Name the blood parasite species.
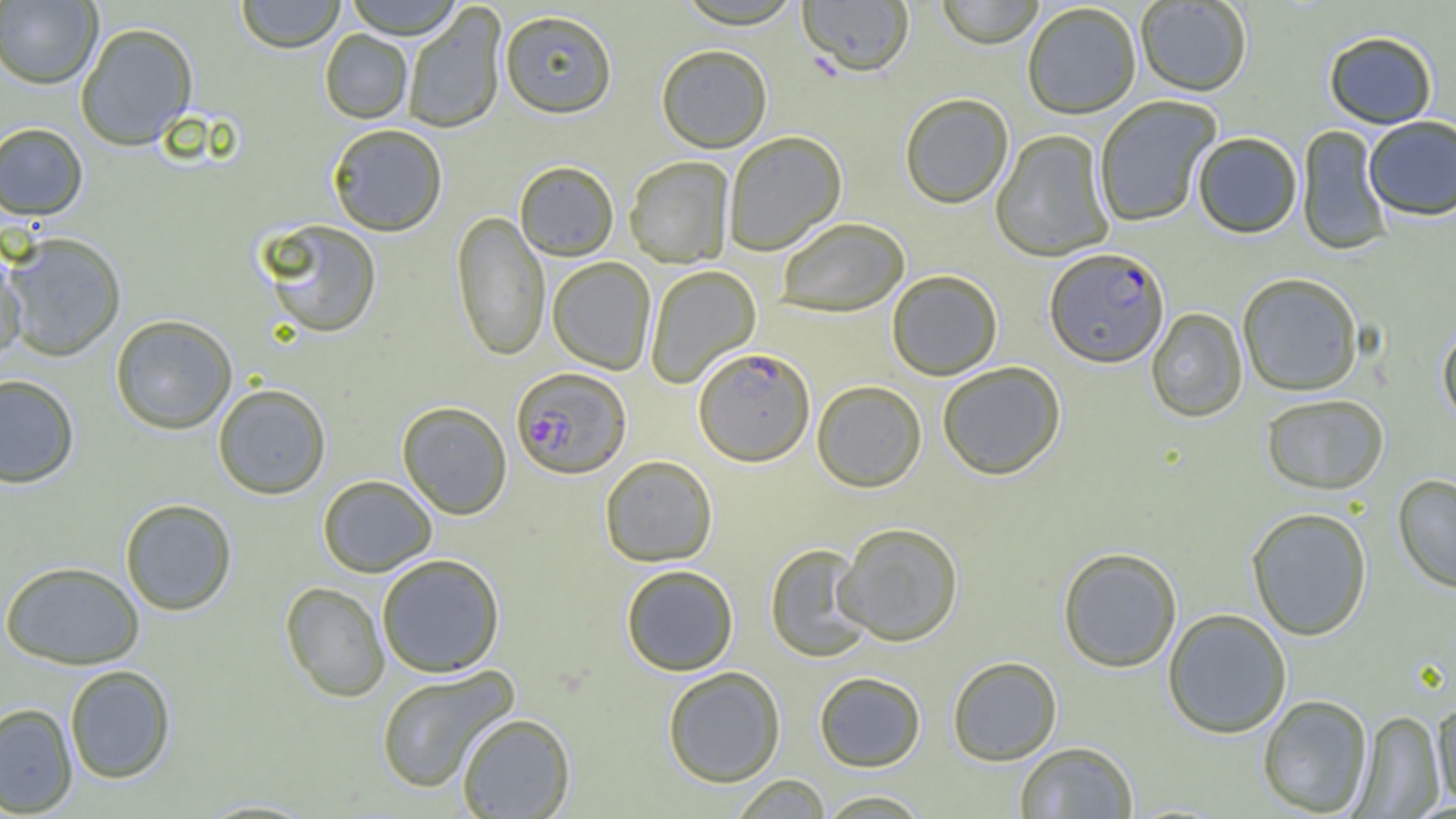

Plasmodium falciparum.

Approximate bounding boxes as (x1, y1, x2, y2) in pixels. Plasmodium falciparum-infected red blood cell locations: (1044, 249, 1169, 370), (693, 347, 815, 467), (510, 366, 631, 480). Uninfected red blood cell locations: (236, 0, 345, 52), (343, 0, 464, 38), (676, 0, 804, 30), (797, 0, 915, 80), (935, 0, 1045, 50), (0, 1, 102, 88), (1136, 1, 1252, 98), (402, 4, 507, 134), (1022, 4, 1141, 121), (499, 10, 618, 119), (75, 22, 198, 150), (320, 29, 413, 123), (1323, 31, 1438, 130), (656, 45, 772, 154), (900, 94, 1014, 210), (1094, 97, 1221, 227), (1364, 118, 1456, 222), (0, 122, 88, 221), (327, 123, 448, 236), (1296, 126, 1393, 257), (992, 131, 1115, 263), (723, 132, 847, 255), (1193, 133, 1302, 239), (624, 157, 734, 268), (514, 161, 619, 261), (452, 210, 550, 362), (777, 218, 910, 317), (258, 219, 383, 338), (2, 232, 127, 362), (0, 248, 27, 365), (547, 257, 656, 375), (645, 265, 761, 389), (887, 271, 1003, 381), (1237, 274, 1363, 397), (1146, 308, 1247, 423), (110, 314, 238, 434), (1437, 322, 1456, 431), (937, 362, 1066, 481), (0, 374, 80, 488), (812, 381, 927, 493), (212, 383, 331, 499), (1261, 395, 1390, 496), (397, 401, 512, 520), (600, 455, 718, 567), (1393, 473, 1456, 594), (317, 474, 438, 577), (119, 498, 237, 615), (1246, 508, 1372, 642), (834, 523, 964, 647), (764, 544, 875, 663), (1057, 548, 1182, 673), (376, 553, 506, 678), (0, 560, 146, 669), (621, 564, 739, 676), (279, 581, 390, 702), (1163, 609, 1292, 739), (948, 656, 1062, 766), (65, 664, 176, 784), (374, 665, 519, 794), (662, 666, 786, 788), (814, 672, 926, 772), (1257, 694, 1373, 817), (1432, 699, 1456, 809), (0, 702, 78, 816), (1354, 710, 1445, 818), (456, 712, 576, 818), (1014, 741, 1138, 818), (729, 774, 832, 818), (816, 790, 932, 818). Thin blood smear. One field of a larger specimen. Image is 1456×819 pixels. Captured at 1000x magnification. Optical microscopy.